Assess this cell for malaria.
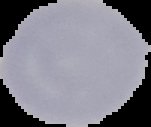
It is uninfected.

Segmented cell region on a black background. Image is 151×127 pixels. From a thin blood smear.